Give the extent of all uninfected red blood cells.
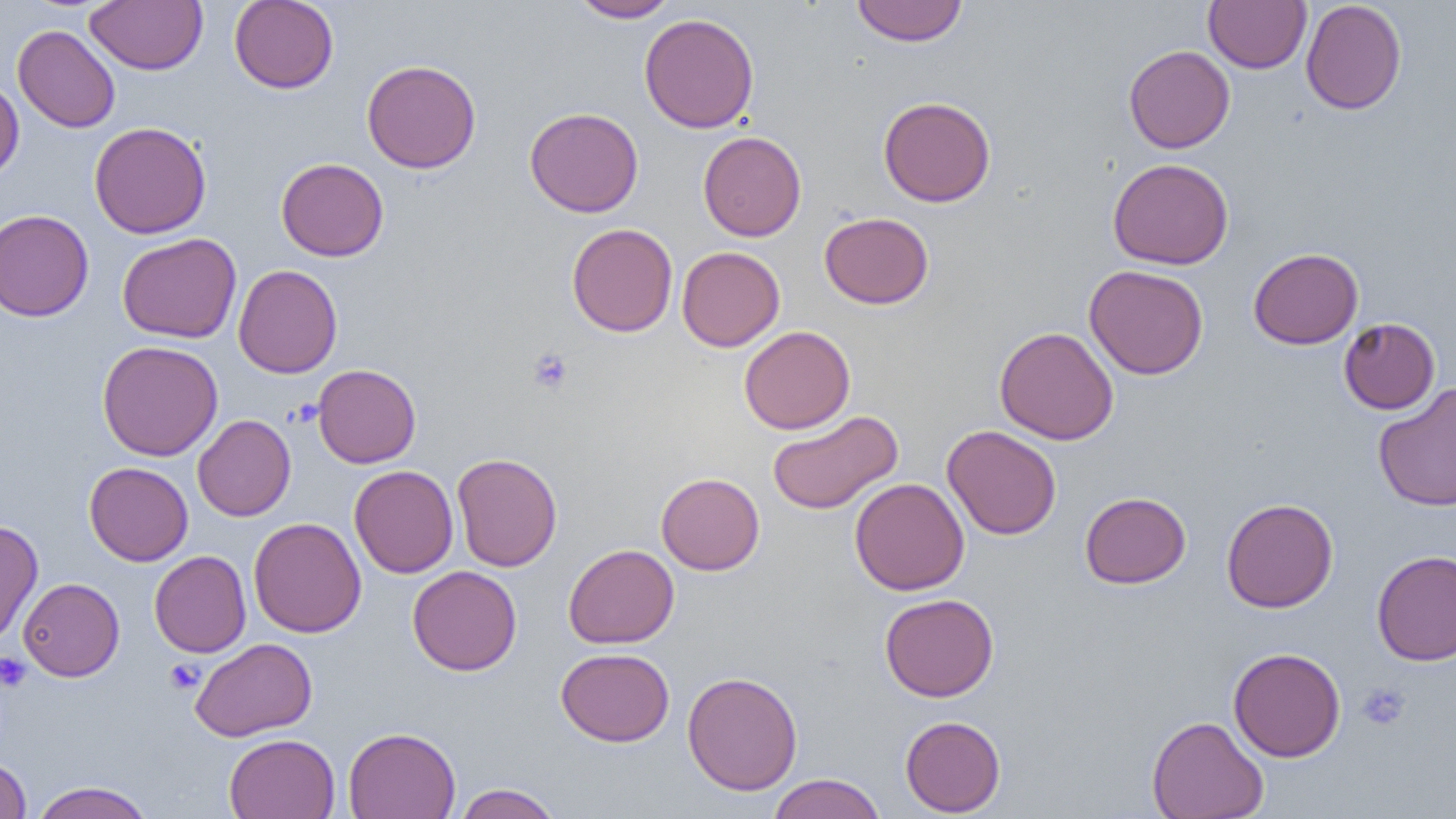

Approximate bounding boxes as named x1/y1/x2/y2 corners in pixels.
Uninfected red blood cells: (x1=85, y1=0, x2=207, y2=74), (x1=229, y1=0, x2=339, y2=93), (x1=569, y1=0, x2=680, y2=23), (x1=851, y1=0, x2=968, y2=46), (x1=1300, y1=0, x2=1407, y2=115), (x1=1203, y1=1, x2=1312, y2=73), (x1=639, y1=13, x2=760, y2=133), (x1=13, y1=25, x2=120, y2=133), (x1=1123, y1=45, x2=1235, y2=153), (x1=362, y1=59, x2=481, y2=173), (x1=0, y1=77, x2=24, y2=183), (x1=878, y1=96, x2=996, y2=207), (x1=524, y1=107, x2=644, y2=217), (x1=88, y1=121, x2=212, y2=238), (x1=698, y1=131, x2=807, y2=241), (x1=276, y1=157, x2=389, y2=261), (x1=1107, y1=157, x2=1234, y2=270), (x1=0, y1=209, x2=94, y2=321), (x1=819, y1=211, x2=934, y2=309), (x1=566, y1=222, x2=678, y2=337), (x1=117, y1=232, x2=242, y2=343), (x1=677, y1=246, x2=785, y2=352), (x1=1249, y1=248, x2=1364, y2=349), (x1=1084, y1=264, x2=1208, y2=380), (x1=233, y1=265, x2=342, y2=378), (x1=1338, y1=317, x2=1440, y2=414), (x1=739, y1=326, x2=855, y2=434), (x1=994, y1=326, x2=1119, y2=445), (x1=97, y1=340, x2=223, y2=461), (x1=312, y1=364, x2=421, y2=468), (x1=1373, y1=384, x2=1456, y2=512), (x1=767, y1=410, x2=903, y2=515), (x1=193, y1=414, x2=296, y2=521), (x1=942, y1=424, x2=1062, y2=540), (x1=452, y1=452, x2=562, y2=571), (x1=84, y1=461, x2=193, y2=566), (x1=349, y1=465, x2=458, y2=578), (x1=656, y1=472, x2=765, y2=575), (x1=850, y1=478, x2=970, y2=595), (x1=1079, y1=491, x2=1192, y2=589), (x1=1221, y1=498, x2=1338, y2=613), (x1=248, y1=516, x2=366, y2=638), (x1=0, y1=520, x2=43, y2=644), (x1=563, y1=544, x2=679, y2=648), (x1=1372, y1=549, x2=1456, y2=666), (x1=149, y1=551, x2=251, y2=657), (x1=407, y1=565, x2=522, y2=675), (x1=18, y1=578, x2=124, y2=681), (x1=879, y1=593, x2=999, y2=701), (x1=190, y1=637, x2=317, y2=741), (x1=556, y1=647, x2=675, y2=746), (x1=1228, y1=647, x2=1346, y2=762), (x1=682, y1=671, x2=804, y2=796), (x1=900, y1=715, x2=1006, y2=817), (x1=1147, y1=715, x2=1269, y2=819), (x1=343, y1=726, x2=461, y2=819), (x1=224, y1=733, x2=340, y2=819), (x1=0, y1=758, x2=32, y2=818), (x1=767, y1=773, x2=886, y2=819), (x1=30, y1=781, x2=155, y2=819), (x1=453, y1=783, x2=563, y2=819).

Platelet locations: (x1=528, y1=348, x2=573, y2=394), (x1=0, y1=653, x2=32, y2=692), (x1=164, y1=658, x2=204, y2=693), (x1=1357, y1=682, x2=1410, y2=731). Slide-level diagnosis: no evidence of blood parasites. Single field of view. Captured at 1000x magnification. Optical microscopy. Image is 1456×819 pixels. Thin blood smear.